State the preparation type.
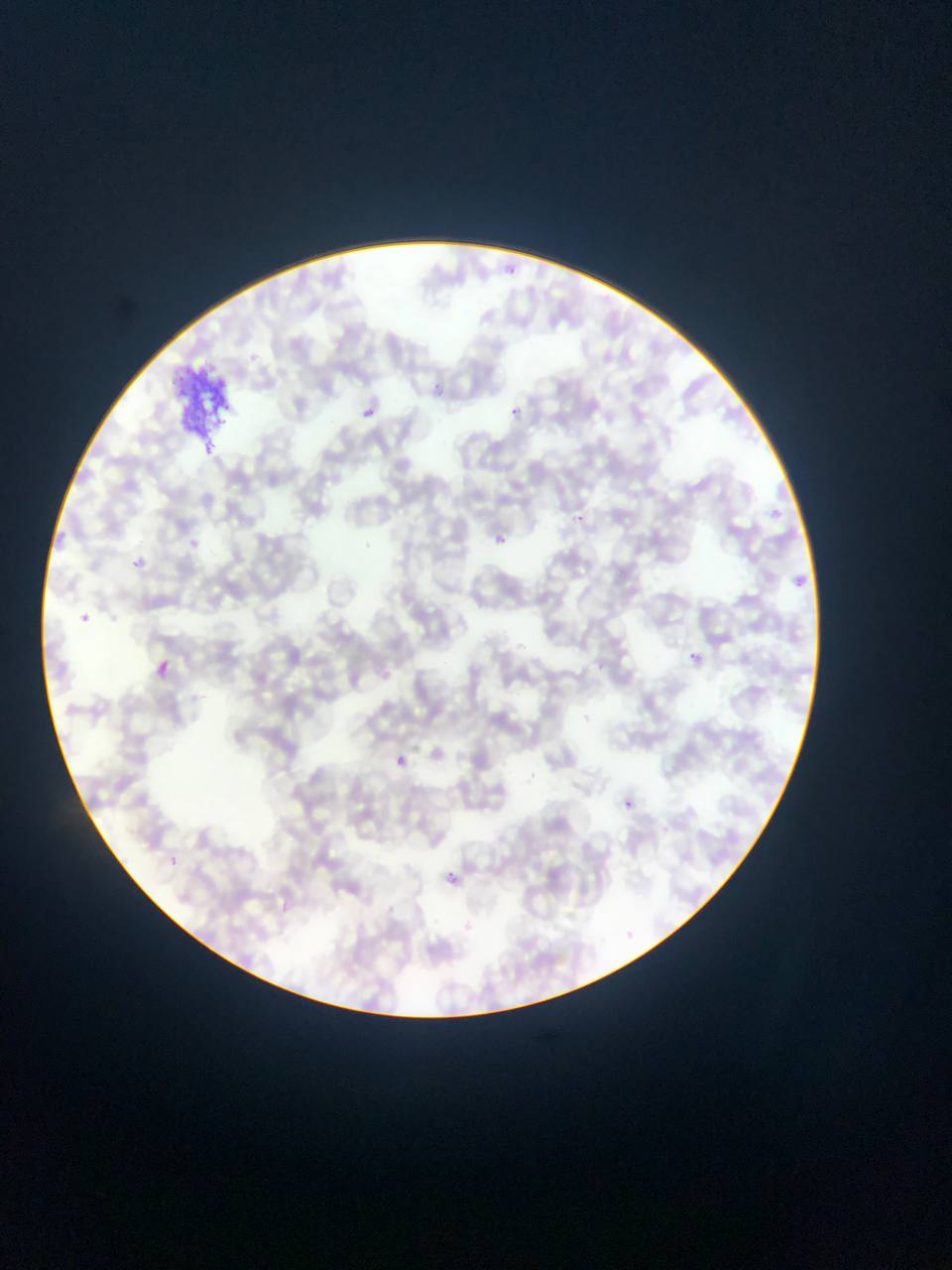

Thin blood smear.

Approximate bounding boxes as (left, top, right, bottom) in pixels. Malaria parasite locations: (434, 380, 442, 392), (358, 404, 386, 419), (511, 404, 521, 424), (575, 510, 583, 523), (490, 531, 512, 543), (185, 540, 195, 551), (127, 549, 152, 573), (76, 613, 97, 627), (686, 649, 703, 664), (155, 659, 169, 676), (395, 755, 406, 767), (624, 799, 634, 808), (169, 855, 183, 869), (441, 869, 461, 886). Artifact (stain precipitate or debris) locations: (165, 361, 244, 446). Sample from Ghana. Image is 952×1270 pixels. Photographed through a microscope with a mobile-phone camera. One field of view.